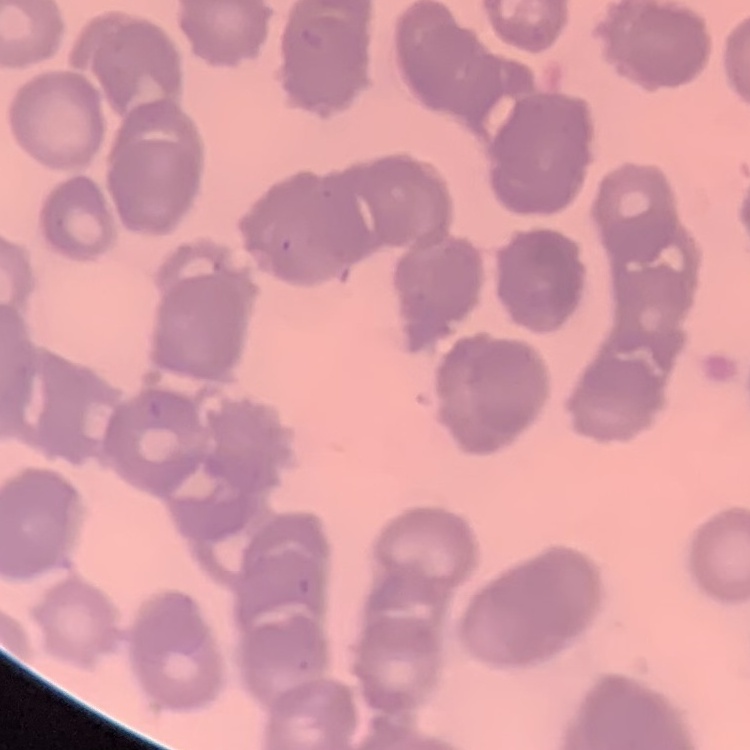 The erythrocytes show rouleaux formation. Square crop of a larger photomicrograph. Stained with either Field's or Giemsa. Thin blood film.